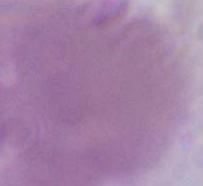

Summary:
  - Magnification: 1000x
  - Modality: micrograph
  - Identification: erythrocyte